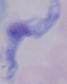
magnification: 1000x
identification: trypanosome
modality: micrograph